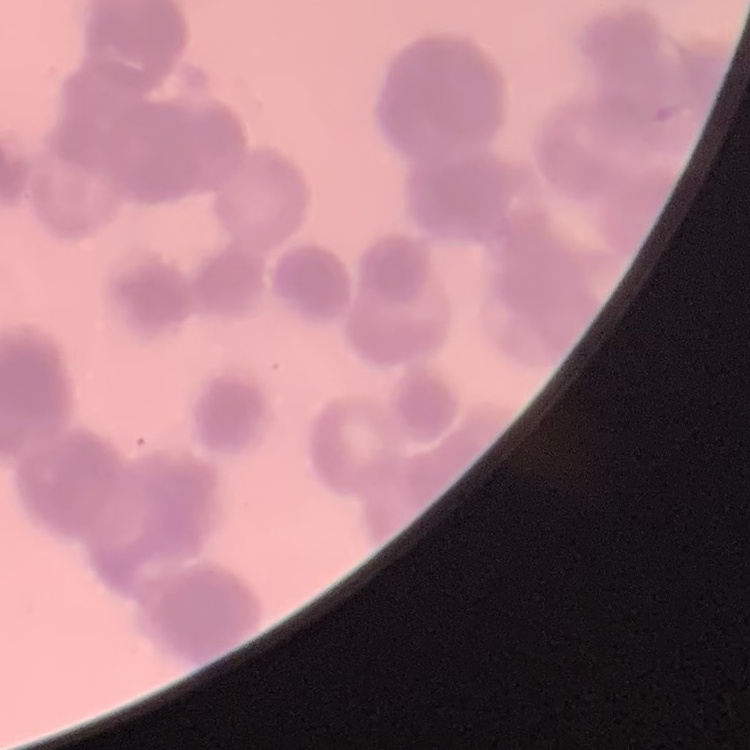 The erythrocytes show rouleaux formation. Thin blood film. Field's or Giemsa stain. One tile cut from a larger photomicrograph.